Draw a bounding box around every parasitised red blood cell, every trophozoite, every gametocyte, every leukocyte, and every artifact (platelet-like body, stain precipitate, or debris).
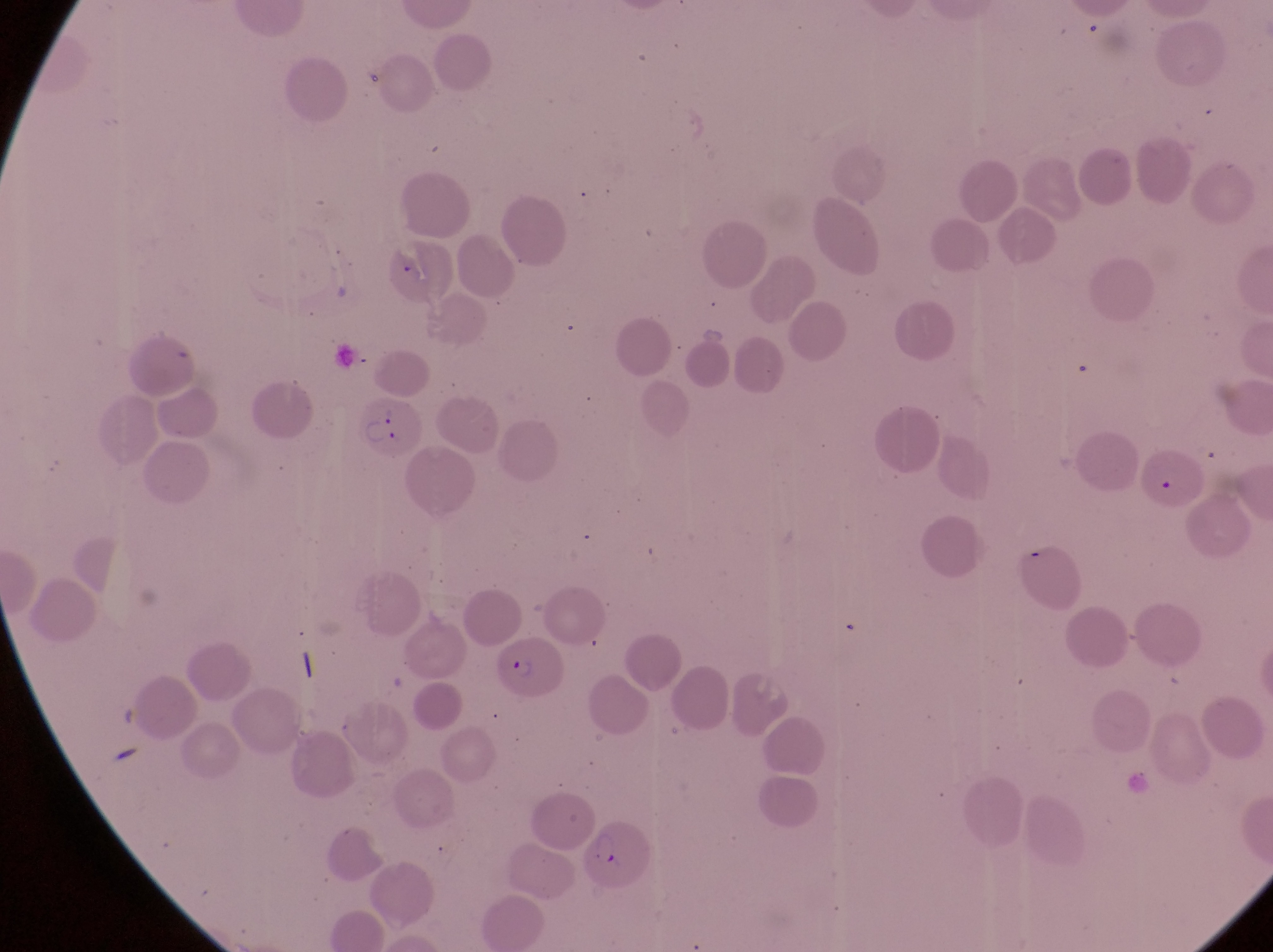
Approximate bounding boxes as [left, top, right, bottom] in pixels.
Parasitised red blood cells: [354, 400, 424, 462], [495, 634, 567, 706], [584, 821, 656, 895].
No leukocytes observed.

Summary:
  - Magnification: 1000x
  - Field of view: single
  - Country: Uganda
  - Preparation: thin blood film
  - Image size: 1273×952 pixels
  - Capture: smartphone photograph through the eyepiece of an Olympus CX-23 microscope